Name the parasite shown.
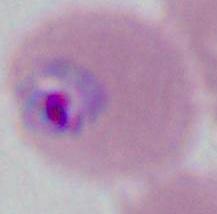
Plasmodium.

Photomicrograph. Captured at either 400x or 1000x magnification.